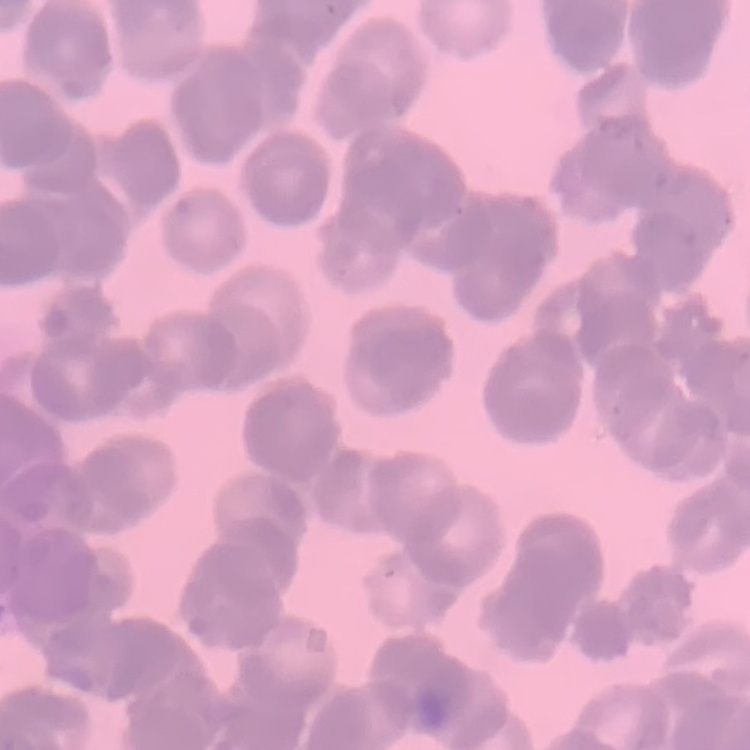 The erythrocytes show rouleaux formation. Thin peripheral smear. Square crop of a larger photomicrograph. Field's or Giemsa stain.